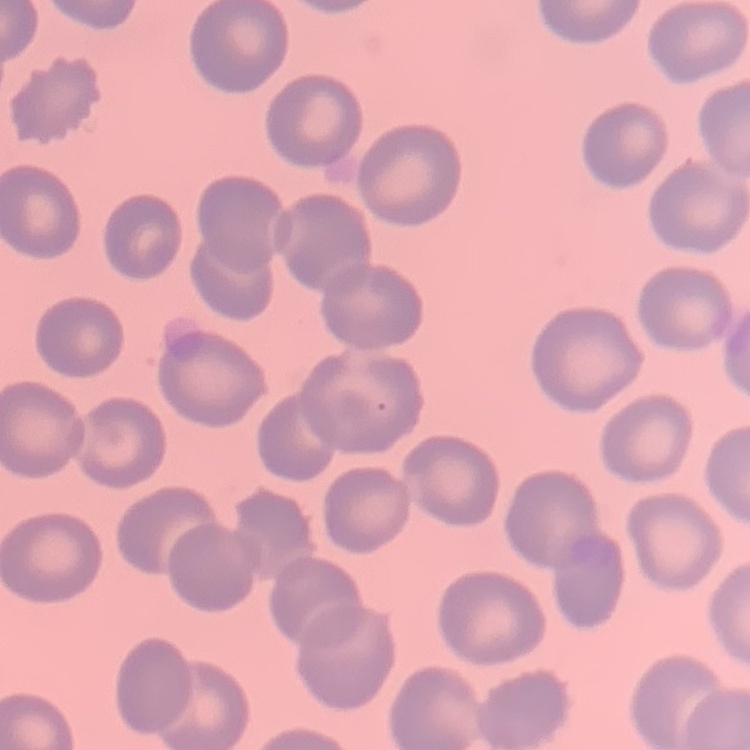

The erythrocytes show no rouleaux formation. Field's or Giemsa stain. Thin peripheral smear. One tile cut from a larger photomicrograph.